State which cell type is depicted.
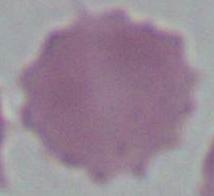
An erythrocyte.

Captured at 1000x magnification. Photomicrograph.